Locate every Plasmodium falciparum-infected red blood cell.
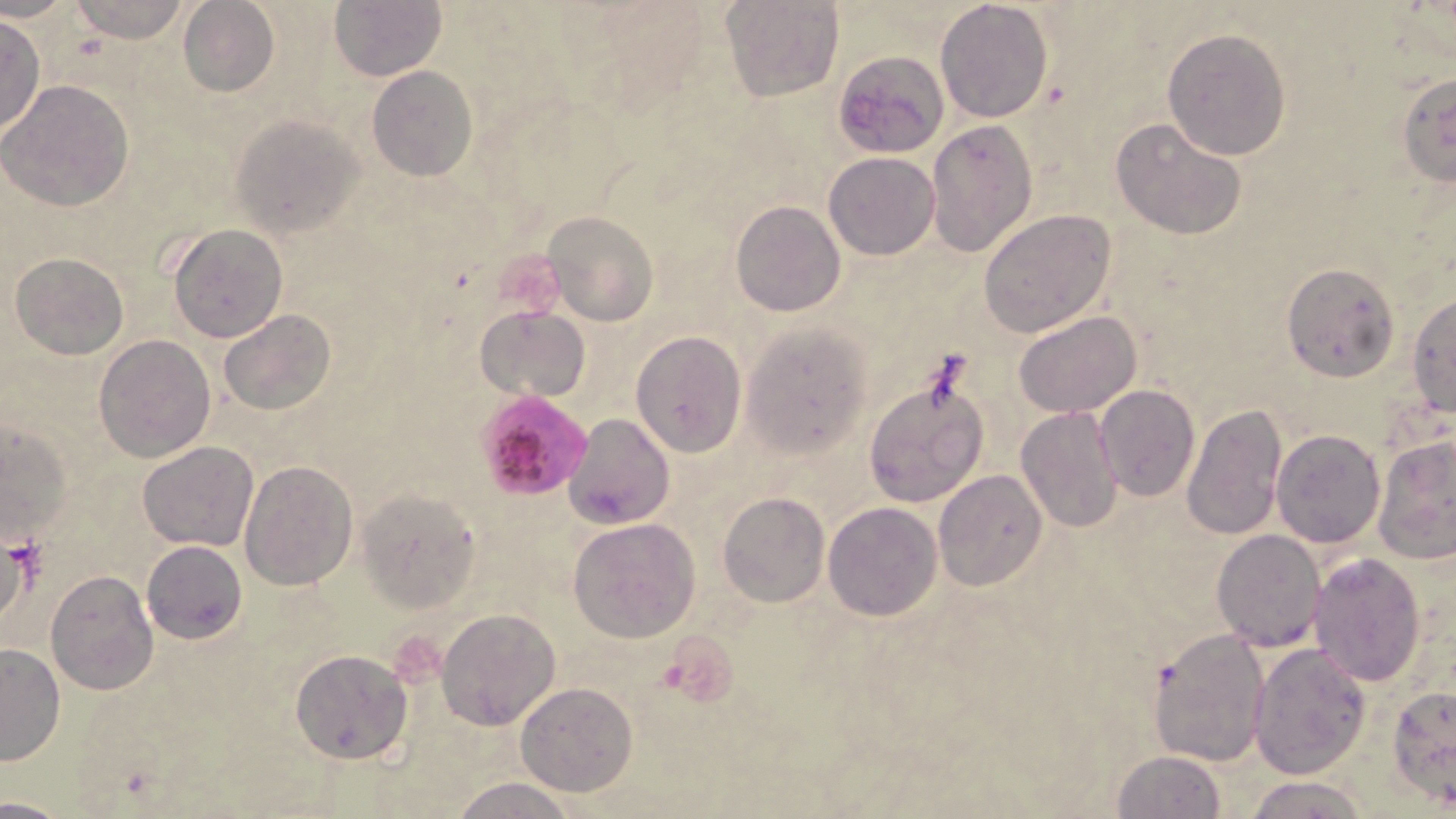

Approximate bounding boxes as named x1/y1/x2/y2 corners in pixels.
Plasmodium falciparum-infected red blood cells: (x1=477, y1=398, x2=607, y2=497).

Uninfected red blood cell locations: (x1=65, y1=0, x2=193, y2=43), (x1=721, y1=0, x2=842, y2=102), (x1=934, y1=0, x2=1053, y2=121), (x1=176, y1=2, x2=280, y2=97), (x1=330, y1=2, x2=445, y2=81), (x1=0, y1=15, x2=47, y2=135), (x1=1162, y1=28, x2=1292, y2=160), (x1=832, y1=52, x2=948, y2=157), (x1=367, y1=65, x2=479, y2=181), (x1=1396, y1=73, x2=1456, y2=188), (x1=1, y1=80, x2=134, y2=212), (x1=232, y1=114, x2=365, y2=236), (x1=1111, y1=117, x2=1247, y2=240), (x1=925, y1=120, x2=1038, y2=258), (x1=824, y1=152, x2=940, y2=259), (x1=730, y1=201, x2=846, y2=317), (x1=978, y1=209, x2=1116, y2=338), (x1=542, y1=210, x2=658, y2=327), (x1=168, y1=224, x2=288, y2=342), (x1=10, y1=251, x2=128, y2=360), (x1=1280, y1=263, x2=1399, y2=382), (x1=1406, y1=294, x2=1455, y2=418), (x1=476, y1=305, x2=590, y2=403), (x1=219, y1=309, x2=336, y2=416), (x1=1013, y1=311, x2=1141, y2=418), (x1=740, y1=322, x2=874, y2=459), (x1=629, y1=331, x2=747, y2=458), (x1=94, y1=334, x2=216, y2=461), (x1=863, y1=372, x2=990, y2=509), (x1=1094, y1=384, x2=1200, y2=501), (x1=1179, y1=402, x2=1287, y2=542), (x1=1014, y1=406, x2=1123, y2=534), (x1=564, y1=413, x2=675, y2=529), (x1=0, y1=423, x2=72, y2=545), (x1=1271, y1=428, x2=1387, y2=548), (x1=1373, y1=434, x2=1455, y2=566), (x1=137, y1=441, x2=257, y2=551), (x1=240, y1=460, x2=358, y2=589), (x1=933, y1=469, x2=1048, y2=589), (x1=356, y1=487, x2=481, y2=613), (x1=718, y1=491, x2=829, y2=607), (x1=823, y1=502, x2=942, y2=621), (x1=568, y1=518, x2=701, y2=642), (x1=1210, y1=527, x2=1327, y2=650), (x1=2, y1=537, x2=45, y2=612), (x1=141, y1=541, x2=247, y2=644), (x1=1308, y1=552, x2=1428, y2=686), (x1=45, y1=570, x2=160, y2=695), (x1=435, y1=608, x2=562, y2=730), (x1=1148, y1=630, x2=1269, y2=767), (x1=1248, y1=641, x2=1371, y2=779), (x1=0, y1=643, x2=64, y2=767), (x1=289, y1=649, x2=413, y2=764), (x1=515, y1=681, x2=640, y2=796), (x1=1388, y1=684, x2=1455, y2=807), (x1=1113, y1=750, x2=1227, y2=818), (x1=1247, y1=774, x2=1370, y2=818), (x1=449, y1=776, x2=582, y2=819), (x1=0, y1=791, x2=66, y2=818). Slide-level diagnosis: Plasmodium falciparum. Thin blood film. Image is 1456×819 pixels. Light microscopy. May-Grünwald-Giemsa-stained preparation. Captured at 1000x magnification. One field of a larger specimen.